Point out each malaria parasite.
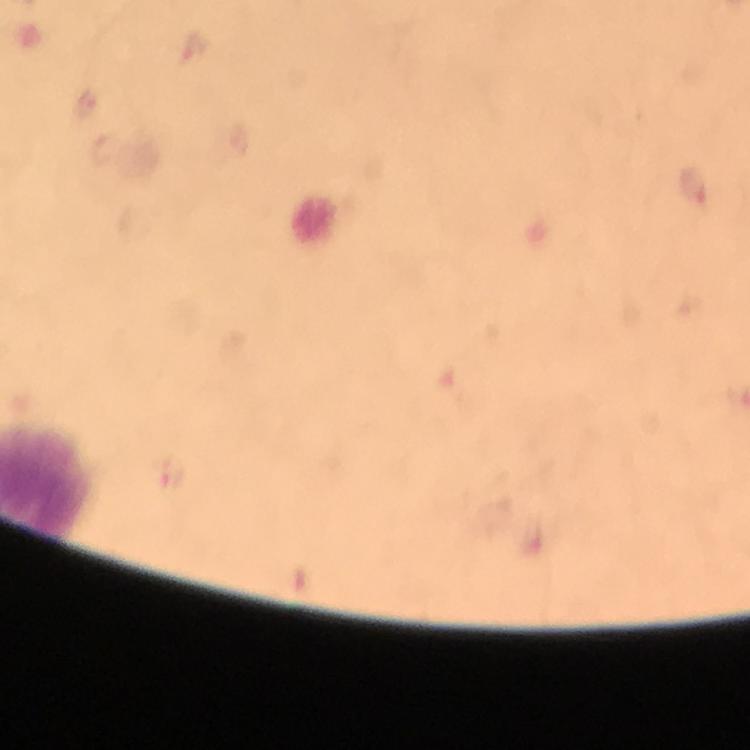

Approximate centers as (x, y) in pixels.
Malaria parasites: (697, 190).

magnification = 100x
preparation = thick blood smear
immersion oil = used
image size = 750×750 pixels
capture = smartphone photograph through a microscope
stain = Giemsa
cropped from = a single field of view
context = from a diagnostic examination for malaria